Classify this cell by malaria status.
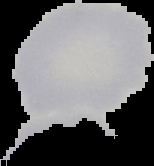

It is uninfected.

From a thin blood smear. Image is 154×166 pixels. The area outside the segmented cell region is set to black.